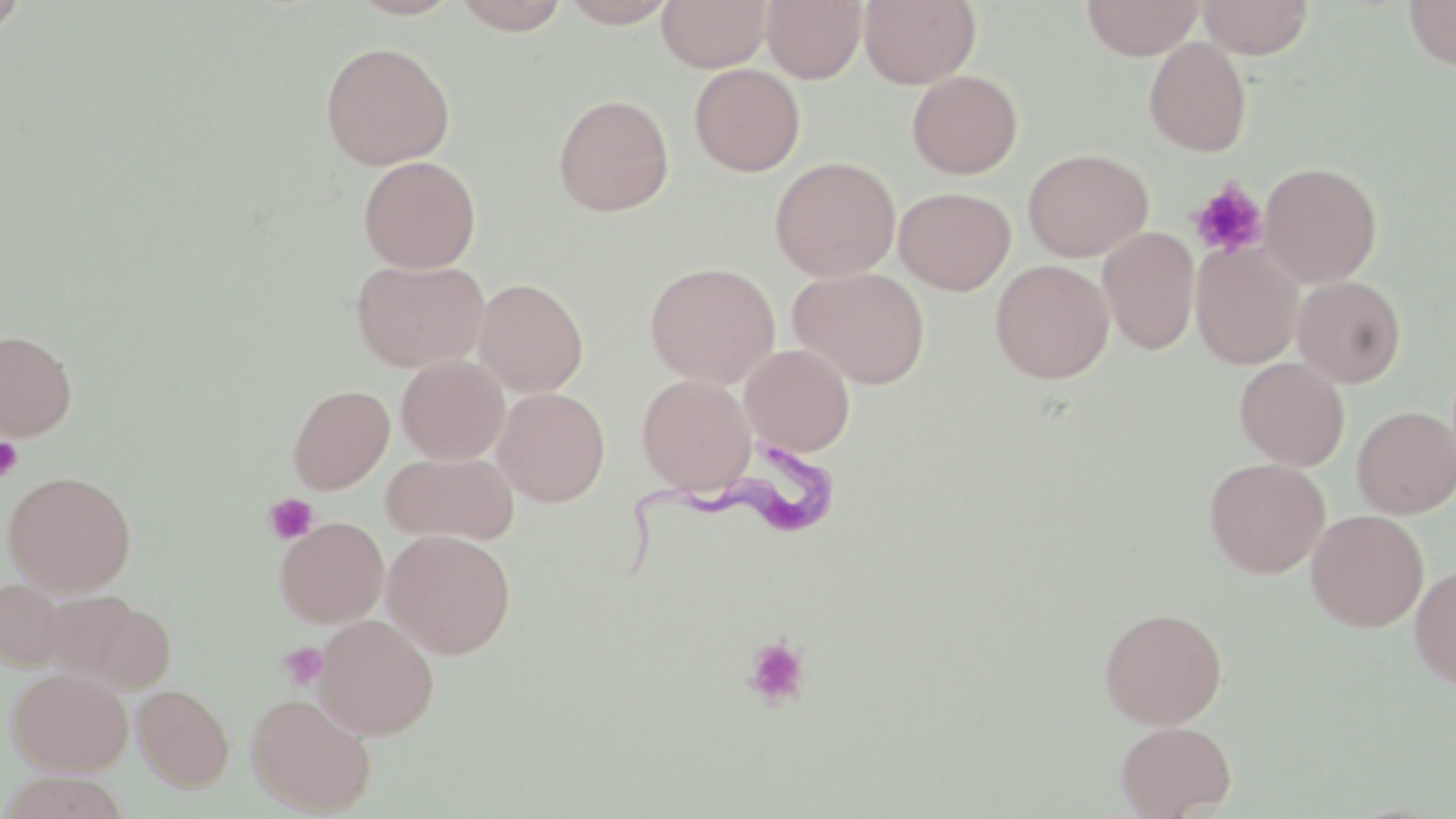
Approximate bounding boxes as (x1, y1, x2, y2) in pixels. Uninfected red blood cell locations: (346, 0, 464, 20), (452, 0, 570, 34), (558, 0, 679, 27), (657, 0, 771, 72), (762, 0, 867, 84), (860, 0, 981, 88), (1081, 0, 1203, 59), (1198, 0, 1315, 58), (1402, 0, 1456, 70), (0, 1, 30, 42), (1143, 37, 1253, 157), (319, 41, 455, 170), (689, 64, 805, 176), (906, 71, 1023, 178), (552, 93, 674, 217), (1022, 148, 1154, 262), (358, 155, 481, 273), (769, 156, 901, 281), (1260, 162, 1382, 286), (894, 187, 1016, 294), (1098, 226, 1200, 355), (1191, 241, 1303, 369), (351, 258, 489, 372), (990, 259, 1114, 383), (644, 262, 781, 388), (789, 267, 930, 389), (1293, 275, 1407, 388), (474, 278, 589, 396), (0, 329, 77, 440), (740, 343, 855, 456), (396, 355, 509, 464), (1234, 358, 1350, 470), (637, 374, 756, 494), (287, 384, 395, 494), (493, 388, 610, 506), (1352, 406, 1456, 518), (381, 451, 519, 545), (1204, 458, 1330, 578), (2, 470, 138, 596), (1306, 510, 1429, 631), (274, 516, 389, 627), (382, 529, 517, 659), (1409, 564, 1456, 689), (0, 578, 67, 671), (37, 590, 145, 684), (86, 602, 177, 694), (1098, 606, 1228, 729), (314, 614, 439, 739), (6, 666, 133, 775), (133, 684, 233, 791), (245, 691, 377, 815), (1115, 720, 1236, 819), (1, 771, 130, 819). Platelet locations: (1188, 180, 1269, 259), (0, 436, 24, 483), (264, 493, 318, 545), (741, 635, 812, 711), (277, 642, 328, 690). Trypanosoma brucei locations: (621, 450, 854, 584). Slide-level diagnosis: Trypanosoma brucei. May-Grünwald-Giemsa-stained preparation. 1000x magnification. One field of a larger specimen. Thin blood film. Optical microscopy. Image is 1456×819 pixels.